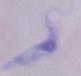

Photomicrograph. A trypanosome is seen. 1000x magnification.